Locate every blood parasite and identify its species.
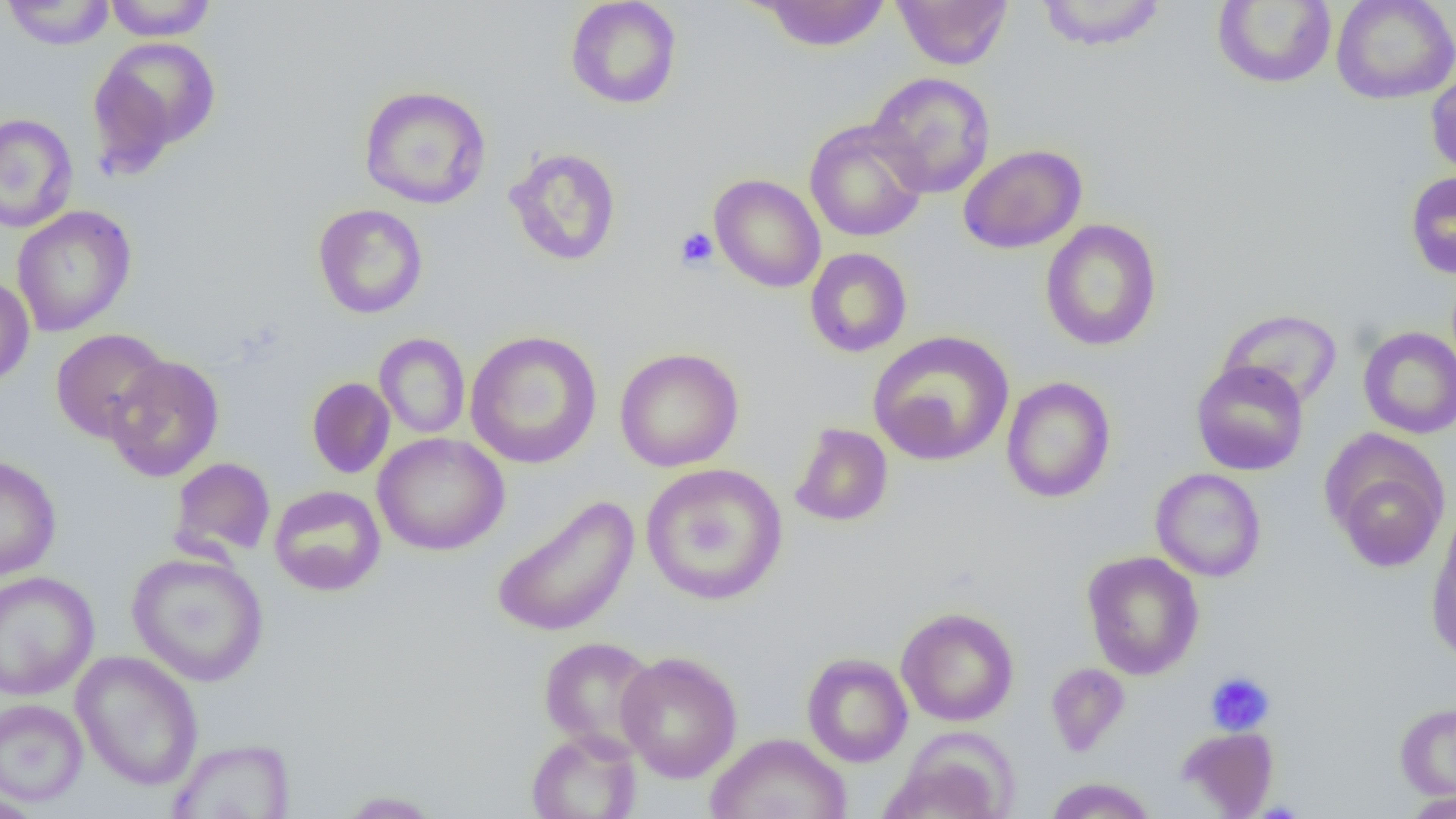
No blood parasites seen.

Approximate bounding boxes as (x1, y1, x2, y2) in pixels. Platelet locations: (675, 227, 718, 271), (1205, 670, 1275, 736). Uninfected red blood cell locations: (104, 0, 217, 41), (565, 0, 683, 109), (754, 0, 893, 52), (891, 0, 1013, 69), (1034, 0, 1167, 51), (1330, 0, 1456, 104), (1, 1, 117, 50), (1212, 2, 1336, 88), (87, 35, 221, 169), (1425, 67, 1456, 180), (867, 72, 995, 198), (358, 84, 492, 209), (0, 113, 78, 233), (804, 120, 929, 242), (958, 144, 1087, 254), (504, 147, 622, 267), (1405, 171, 1456, 280), (709, 174, 825, 293), (313, 203, 428, 319), (11, 205, 137, 337), (1040, 219, 1162, 352), (804, 248, 912, 358), (0, 274, 35, 388), (1217, 308, 1342, 409), (1358, 326, 1456, 439), (50, 328, 170, 443), (464, 330, 603, 469), (867, 330, 1014, 467), (374, 333, 470, 439), (614, 347, 744, 472), (104, 354, 224, 483), (1191, 360, 1309, 476), (1000, 376, 1116, 503), (306, 377, 395, 479), (789, 423, 893, 527), (373, 432, 509, 556), (1327, 446, 1448, 573), (0, 455, 62, 580), (169, 456, 276, 560), (640, 463, 788, 606), (1150, 468, 1266, 582), (269, 485, 386, 596), (490, 494, 640, 638), (1425, 525, 1456, 663), (1081, 551, 1204, 679), (127, 552, 270, 687), (0, 571, 99, 701), (896, 607, 1019, 726), (538, 636, 660, 756), (71, 650, 204, 791), (615, 651, 743, 783), (802, 652, 913, 767), (1045, 662, 1130, 757), (0, 698, 88, 806), (1395, 700, 1456, 803), (1177, 726, 1279, 817), (525, 729, 642, 818), (705, 732, 852, 819), (885, 736, 1017, 819), (168, 738, 296, 818), (1044, 777, 1158, 818), (1401, 789, 1456, 818), (336, 790, 443, 818), (0, 791, 43, 819). Slide-level diagnosis: negative for blood parasites. Thin blood film. Captured at 1000x magnification. Optical microscopy. Image is 1456×819 pixels. One field of a larger specimen.